Name the parasite shown.
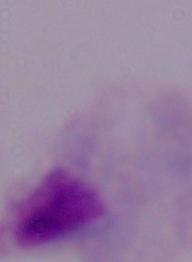

This is a trichomonad.

Summary:
  - Modality: micrograph
  - Magnification: 1000x